Identify the parasite.
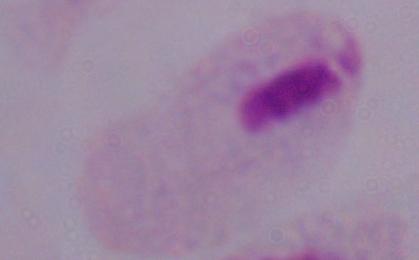

A trichomonad.

Summary:
  - Magnification: 1000x
  - Modality: micrograph